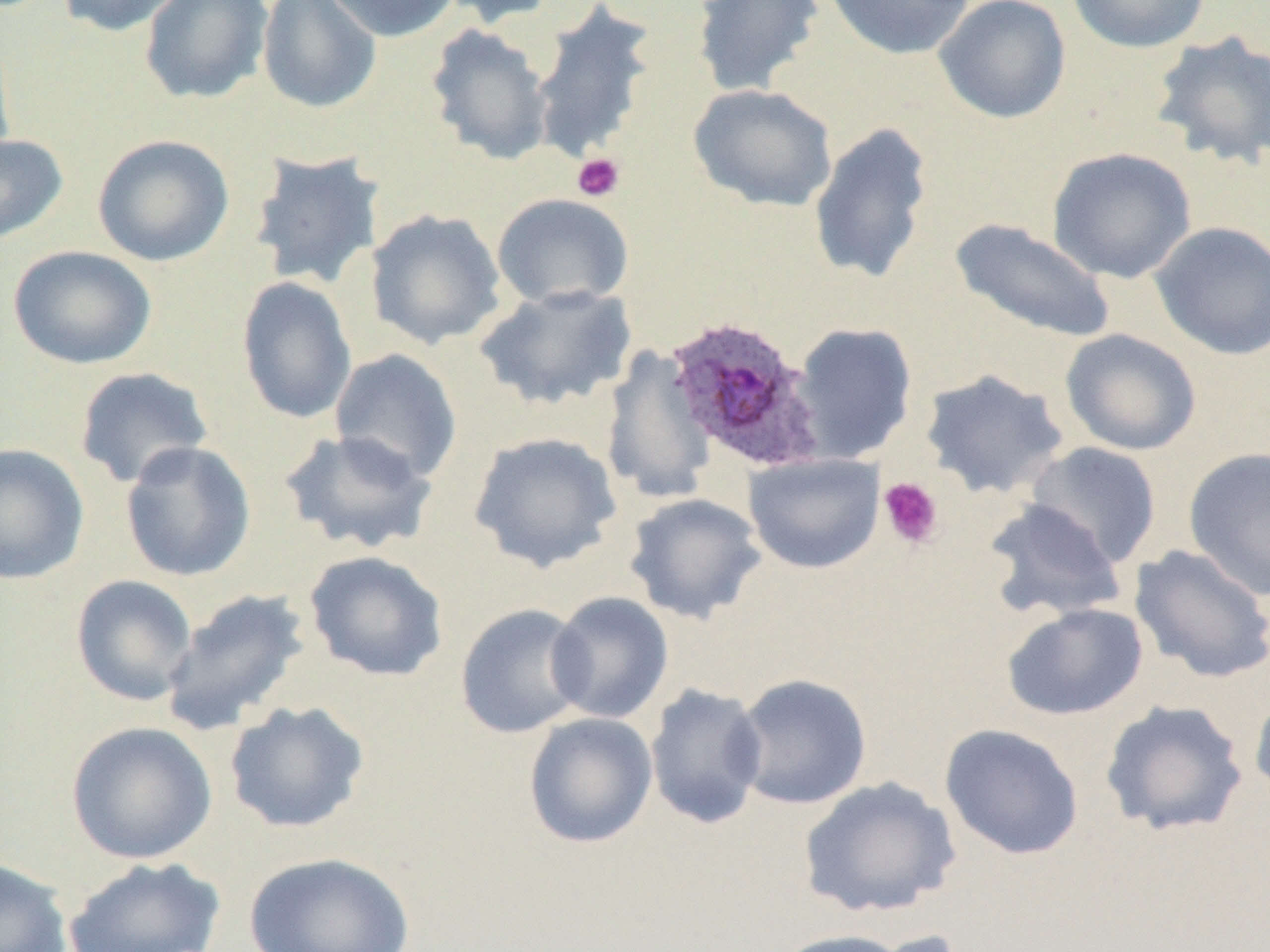 Approximate bounding boxes as [x1, y1, x2, y2] in pixels. Platelet locations: [571, 153, 625, 202], [878, 476, 944, 550]. Uninfected red blood cell locations: [58, 0, 187, 37], [139, 0, 274, 106], [257, 0, 382, 114], [320, 0, 461, 42], [435, 0, 563, 27], [823, 0, 976, 60], [933, 0, 1072, 124], [1066, 0, 1212, 54], [691, 1, 825, 98], [529, 3, 659, 165], [425, 23, 555, 166], [0, 29, 16, 174], [1150, 31, 1270, 170], [688, 83, 838, 212], [807, 121, 935, 287], [0, 134, 68, 244], [92, 134, 234, 267], [1047, 147, 1197, 284], [248, 149, 385, 290], [491, 193, 635, 310], [365, 208, 507, 350], [948, 218, 1117, 345], [1150, 221, 1270, 360], [8, 245, 157, 370], [236, 276, 357, 425], [474, 282, 638, 411], [790, 322, 918, 462], [1060, 328, 1202, 456], [600, 346, 718, 505], [329, 348, 463, 484], [73, 366, 214, 489], [919, 368, 1069, 500], [277, 428, 438, 555], [468, 431, 623, 574], [120, 440, 257, 582], [0, 442, 90, 584], [1023, 442, 1163, 568], [1183, 447, 1270, 600], [744, 453, 885, 574], [623, 492, 767, 625], [981, 499, 1128, 621], [1129, 544, 1270, 684], [304, 550, 449, 681], [70, 574, 198, 706], [159, 587, 313, 737], [546, 591, 674, 724], [1002, 602, 1148, 721], [455, 603, 591, 739], [731, 673, 872, 810], [645, 683, 768, 830], [1248, 684, 1270, 806], [1100, 698, 1250, 837], [224, 700, 370, 835], [523, 711, 658, 849], [65, 721, 218, 865], [939, 723, 1084, 860], [798, 776, 962, 919], [242, 850, 415, 952], [63, 856, 226, 952], [0, 857, 73, 952], [770, 928, 914, 952], [856, 928, 973, 952]. Plasmodium ovale-infected red blood cell locations: [664, 316, 825, 471]. Slide-level diagnosis: Plasmodium ovale. One field of a larger specimen. Optical microscopy. Image is 1270×952 pixels. Thin blood smear. Captured at 1000x magnification.